Assess this cell for malaria.
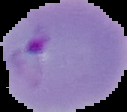
Parasitized.

Summary:
  - Image type: cell region segmented out of the field of view; surrounding area masked to black
  - Image size: 127×112 pixels
  - Preparation: thin blood smear